Give a bounding box for every leukocyte visible.
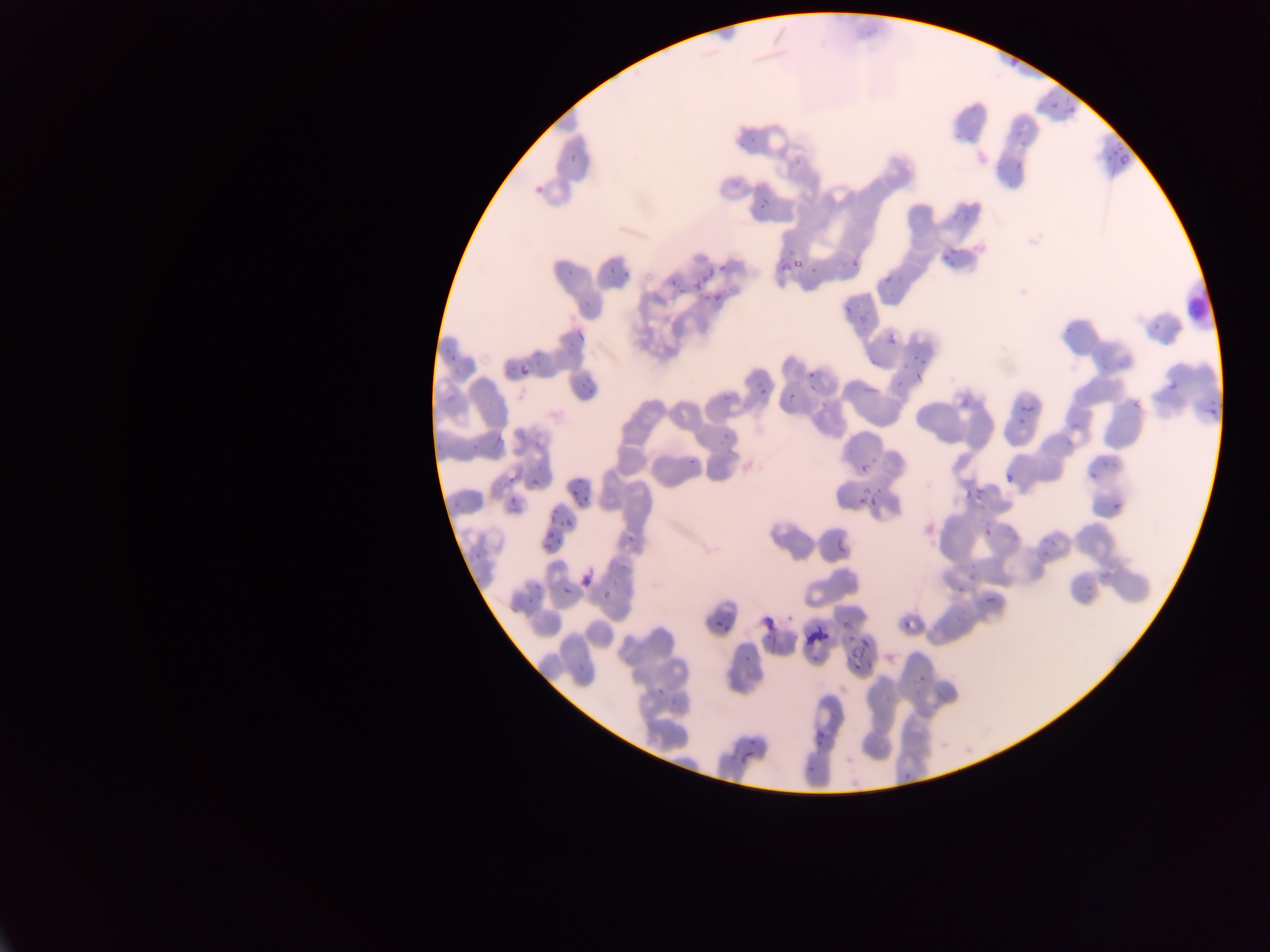

No leukocytes observed.

Approximate bounding boxes as (left, top, right, bottom) in pixels.
Summary:
  - Malaria parasite locations: (1003, 49, 1026, 73), (1050, 102, 1059, 110), (1069, 106, 1080, 117), (1012, 125, 1025, 137), (1114, 142, 1124, 153), (1017, 144, 1030, 150), (1109, 147, 1116, 157), (563, 151, 579, 162), (1105, 154, 1111, 162), (1118, 155, 1129, 165), (1013, 159, 1027, 172), (533, 182, 550, 200), (757, 201, 767, 211), (951, 244, 958, 258), (942, 254, 952, 260), (852, 260, 863, 268), (948, 261, 956, 270), (563, 263, 573, 276), (717, 263, 727, 272), (606, 264, 619, 275), (622, 269, 632, 277), (700, 271, 712, 283), (879, 273, 892, 284), (668, 275, 677, 285), (695, 281, 702, 292), (678, 287, 688, 298), (712, 291, 723, 302), (1152, 323, 1160, 331), (570, 330, 588, 339), (885, 331, 900, 347), (449, 353, 460, 359), (515, 361, 530, 375), (805, 370, 813, 380), (913, 371, 922, 379), (1166, 377, 1183, 390), (578, 382, 588, 390), (583, 385, 596, 396), (759, 389, 768, 398), (722, 390, 731, 401), (785, 393, 796, 404), (1132, 399, 1140, 406), (1208, 399, 1217, 406), (1018, 400, 1028, 415), (819, 403, 830, 410), (1028, 408, 1037, 416), (1207, 409, 1216, 419), (1018, 415, 1027, 426), (1070, 418, 1083, 428), (720, 430, 734, 444), (470, 441, 481, 451), (687, 455, 699, 466), (861, 465, 866, 474), (505, 471, 521, 487), (1004, 472, 1018, 482), (1087, 473, 1097, 478), (531, 477, 544, 487), (579, 480, 587, 488), (975, 487, 984, 496), (569, 489, 579, 496), (963, 489, 968, 498), (578, 492, 594, 507), (506, 495, 522, 512), (870, 498, 878, 507), (856, 501, 864, 505), (1112, 501, 1121, 510), (551, 507, 561, 514), (548, 515, 563, 522), (566, 517, 577, 527), (984, 525, 993, 537), (542, 530, 559, 552), (627, 536, 637, 545), (837, 541, 845, 552), (471, 553, 483, 560), (578, 571, 594, 590), (561, 581, 572, 596), (533, 582, 543, 590), (954, 585, 964, 592), (526, 597, 533, 605), (985, 597, 996, 603), (785, 613, 794, 622), (841, 614, 859, 631), (902, 621, 907, 632), (714, 622, 723, 629), (764, 633, 774, 639), (846, 642, 864, 659), (743, 656, 752, 663), (852, 661, 863, 669), (918, 676, 926, 682), (813, 728, 828, 742), (747, 738, 756, 745), (741, 753, 756, 760), (806, 762, 817, 775) | approximate (x, y) pixel centers of objects too small to bound: (752, 138), (704, 299), (848, 310), (917, 356), (904, 366), (864, 491), (880, 491), (1046, 538), (1044, 554), (605, 597), (726, 630), (660, 690), (906, 776)
  - Country: Ghana
  - Preparation: thin blood smear
  - Capture: mobile-phone photograph through a microscope
  - Image size: 1270×952 pixels
  - Field of view: single